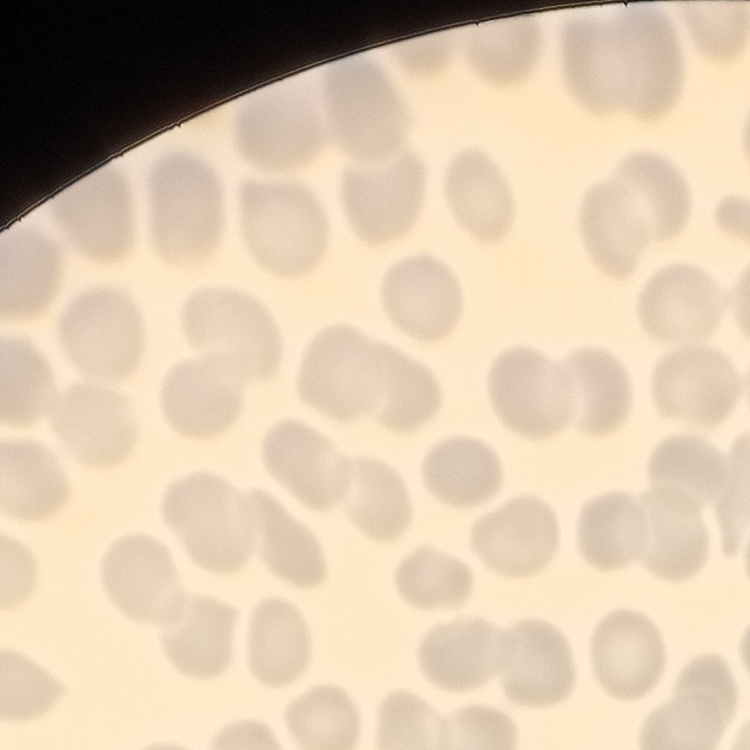
red_blood_cell_morphology: no rouleaux formation
stain: Field's or Giemsa
image_type: one tile cut from a larger photomicrograph
preparation: thin blood film